Report the malaria status of this cell.
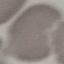
It is uninfected.

capture: smartphone through the microscope eyepiece
preparation: thin blood film
image_type: automatically extracted cell patch, resized to 64 × 64 pixels
stain: Giemsa